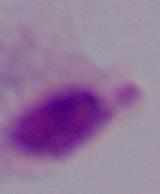

Summary:
  - Modality: photomicrograph
  - Magnification: 1000x
  - Identification: trichomonad